Point out each Plasmodium parasite.
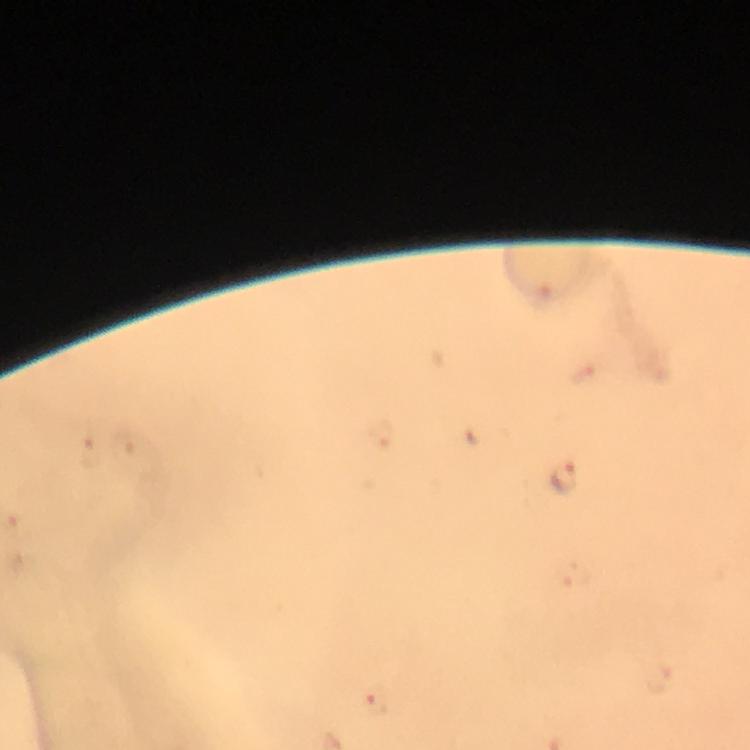
Approximate centers as (x, y) in pixels.
Plasmodium parasites: (566, 479), (377, 703).

{
  "capture": "smartphone camera through the microscope",
  "immersion_oil": "used",
  "preparation": "thick blood smear",
  "stain": "Giemsa",
  "magnification": "100x",
  "cropped_from": "one field of view",
  "image_size": "750×750 pixels",
  "context": "from a malaria diagnostic workup"
}